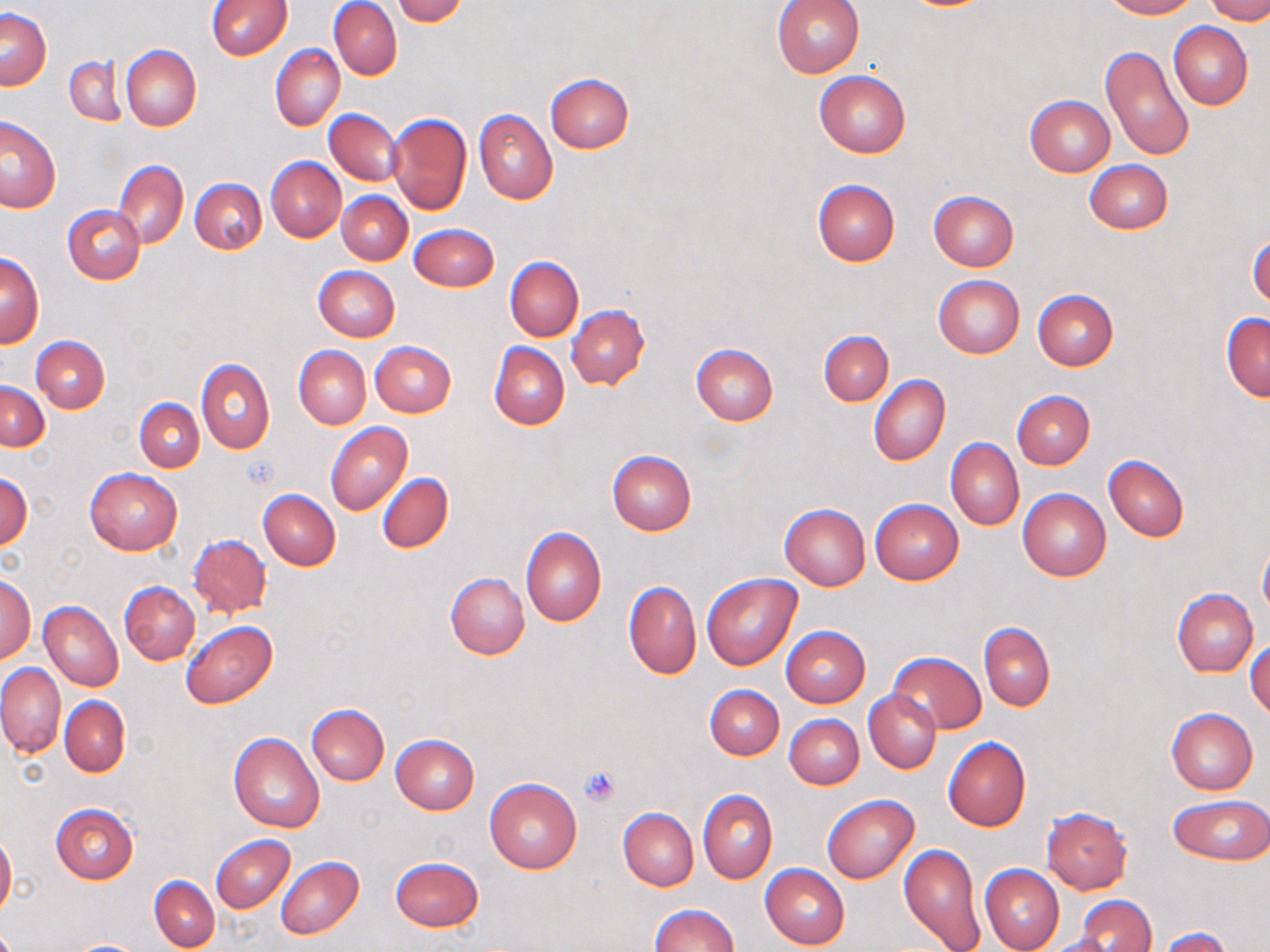

slide-level diagnosis = negative for blood parasites
stain = May-Grünwald-Giemsa
platelet locations = approximate bounding boxes as (x1, y1, x2, y2) in pixels: (241, 453, 279, 489), (579, 765, 622, 808)
image size = 1270×952 pixels
uninfected red blood cell locations = approximate bounding boxes as (x1, y1, x2, y2) in pixels: (393, 0, 470, 25), (772, 0, 865, 78), (1101, 0, 1199, 19), (1206, 0, 1270, 24), (207, 1, 291, 60), (330, 2, 402, 80), (1, 9, 51, 90), (1168, 22, 1252, 111), (271, 44, 345, 130), (1101, 44, 1195, 162), (121, 46, 201, 130), (64, 55, 127, 127), (813, 71, 910, 159), (545, 73, 634, 152), (1024, 94, 1115, 176), (474, 108, 557, 204), (324, 109, 403, 185), (386, 113, 472, 215), (1, 116, 61, 212), (266, 157, 345, 241), (113, 159, 188, 248), (1084, 159, 1173, 234), (190, 178, 266, 255), (812, 180, 900, 265), (338, 190, 413, 265), (928, 190, 1018, 272), (63, 205, 146, 284), (408, 224, 499, 292), (1248, 235, 1270, 309), (1, 253, 44, 347), (504, 256, 583, 341), (313, 266, 400, 342), (933, 275, 1025, 358), (1033, 289, 1118, 370), (566, 305, 649, 389), (1221, 312, 1269, 401), (818, 329, 893, 406), (30, 335, 110, 413), (371, 341, 457, 417), (488, 341, 569, 431), (690, 343, 778, 426), (294, 346, 370, 429), (195, 358, 273, 454), (868, 374, 950, 466), (1, 382, 49, 451), (1012, 390, 1095, 469), (135, 398, 204, 471), (326, 422, 413, 516), (946, 437, 1024, 531), (607, 450, 696, 534), (1103, 455, 1189, 541), (86, 468, 182, 555), (377, 472, 454, 554), (0, 474, 32, 549), (1018, 489, 1111, 580), (258, 490, 340, 571), (869, 499, 964, 585), (779, 504, 870, 590), (520, 526, 605, 627), (188, 534, 272, 617), (1259, 541, 1270, 620), (445, 572, 530, 659), (1, 573, 36, 666), (701, 574, 802, 670), (623, 581, 701, 679), (119, 582, 200, 664), (1172, 588, 1258, 676), (39, 601, 123, 691), (181, 621, 278, 708), (978, 623, 1056, 710), (781, 626, 870, 706), (1246, 640, 1270, 721), (887, 652, 984, 735), (0, 663, 65, 756), (704, 684, 784, 759), (864, 690, 941, 772), (60, 696, 130, 776), (306, 703, 390, 785), (1165, 708, 1258, 794), (783, 715, 864, 789), (229, 732, 326, 833), (391, 734, 479, 814), (943, 737, 1031, 831), (484, 778, 583, 874), (698, 789, 778, 883), (822, 794, 919, 883), (1169, 795, 1270, 865), (50, 803, 138, 883), (1041, 807, 1132, 894), (618, 808, 699, 890), (0, 832, 17, 917), (211, 834, 295, 913), (898, 843, 987, 952), (275, 856, 364, 940), (389, 856, 485, 931), (760, 864, 850, 949), (979, 864, 1064, 952), (148, 876, 220, 951), (1076, 896, 1156, 952), (648, 904, 738, 952), (1159, 927, 1232, 952), (1039, 932, 1124, 952), (65, 939, 150, 951)
magnification = 1000x
field of view = one of a larger specimen
preparation = thin blood film
modality = optical microscopy